Classify this cell by malaria status.
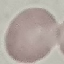

Uninfected.

Summary:
  - Stain: Giemsa
  - Image type: automatically extracted cell patch, resized to 64 × 64 pixels
  - Capture: smartphone camera at the microscope eyepiece
  - Preparation: thin blood smear